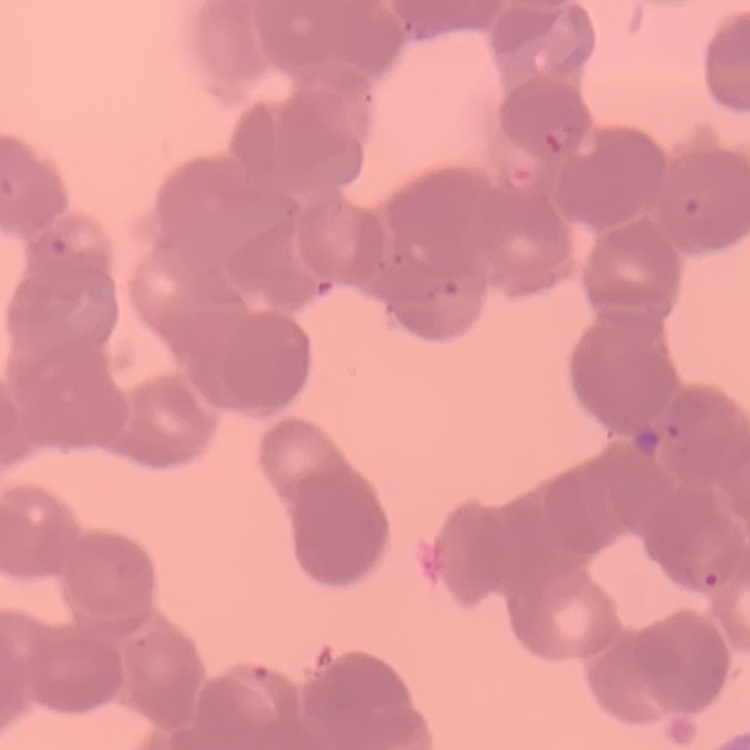

red blood cell morphology = rouleaux formation
preparation = thin blood smear
stain = Field's or Giemsa
image type = one tile cut from a larger photomicrograph